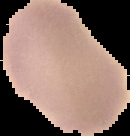 Malaria status: uninfected. From a thin blood film. Image is 130×136 pixels. Segmented cell region on a black background.